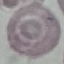
Malaria status: uninfected. Photographed with a smartphone camera at the microscope eyepiece. Cell patch, automatically extracted from a larger field of view and resized to 64 × 64 pixels. Thin blood smear. Giemsa-stained preparation.